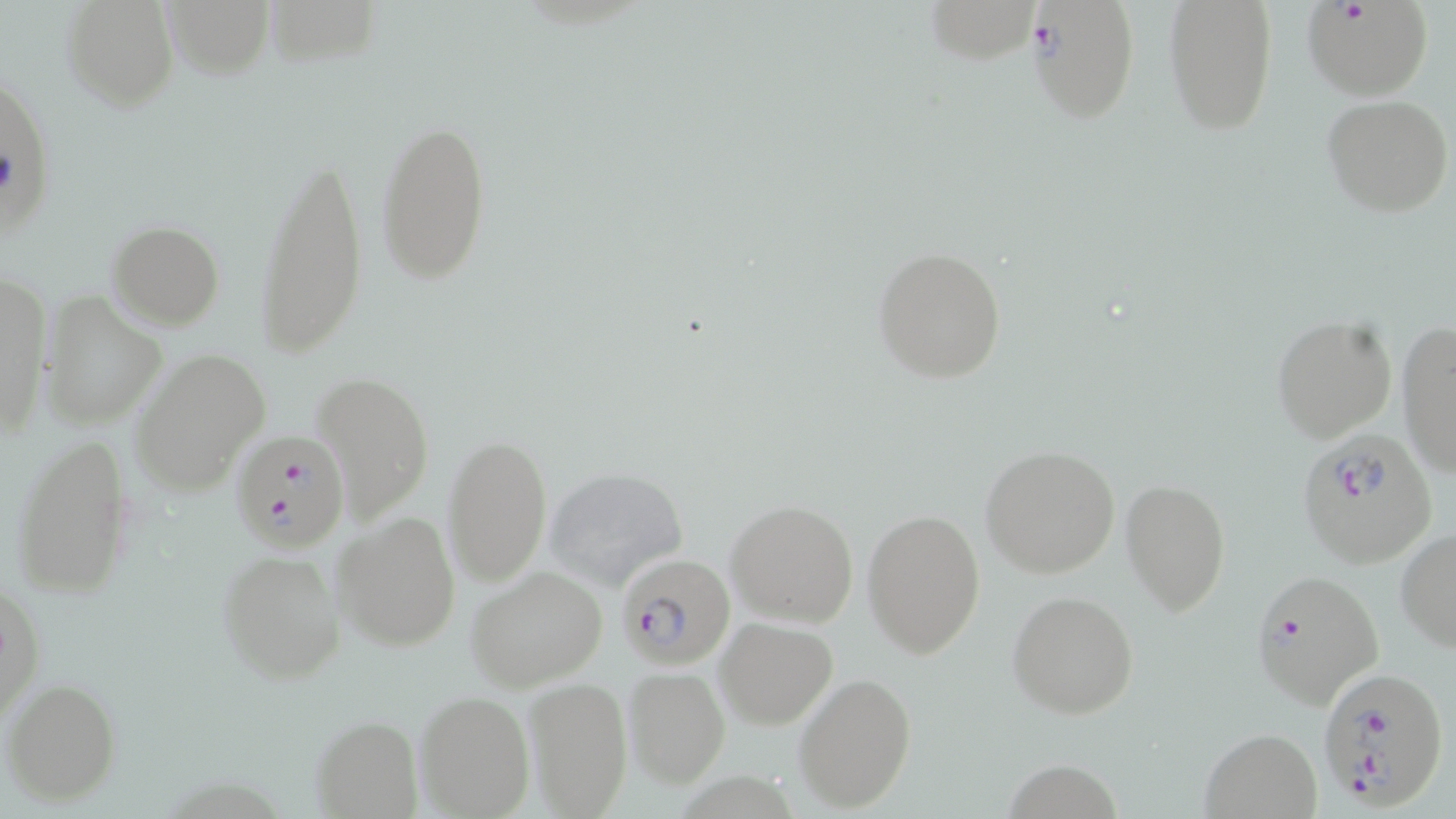

Summary:
  - Coordinate format: approximate bounding boxes as [x1, y1, x2, y2] in pixels
  - Uninfected red blood cell locations: [61, 0, 180, 112], [163, 0, 273, 79], [260, 0, 379, 71], [926, 0, 1040, 64], [1164, 0, 1278, 135], [1322, 94, 1453, 217], [374, 114, 490, 288], [258, 145, 367, 364], [106, 220, 227, 331], [871, 245, 1007, 384], [0, 271, 50, 440], [39, 294, 166, 430], [1271, 315, 1397, 443], [1396, 321, 1456, 479], [130, 347, 270, 495], [314, 371, 433, 520], [443, 431, 553, 587], [9, 432, 136, 601], [980, 444, 1120, 579], [540, 465, 691, 591], [1121, 477, 1230, 615], [725, 498, 860, 627], [863, 505, 985, 661], [333, 509, 460, 653], [1395, 528, 1456, 653], [215, 546, 345, 685], [463, 565, 610, 692], [1, 581, 44, 722], [1008, 589, 1139, 719], [715, 616, 837, 729], [623, 665, 730, 786], [794, 673, 917, 812], [522, 676, 634, 818], [4, 679, 120, 805], [414, 690, 536, 819], [312, 716, 421, 819], [1198, 728, 1323, 819]
  - Plasmodium falciparum-infected red blood cell locations: [1025, 0, 1139, 123], [1306, 3, 1433, 99], [229, 428, 351, 554], [1296, 429, 1438, 568], [617, 553, 735, 670], [1250, 569, 1385, 709], [1316, 667, 1449, 810]
  - Slide-level diagnosis: Plasmodium falciparum
  - Field of view: single
  - Magnification: 1000x
  - Preparation: thin blood smear
  - Image size: 1456×819 pixels
  - Modality: light microscopy
  - Stain: May-Grünwald-Giemsa